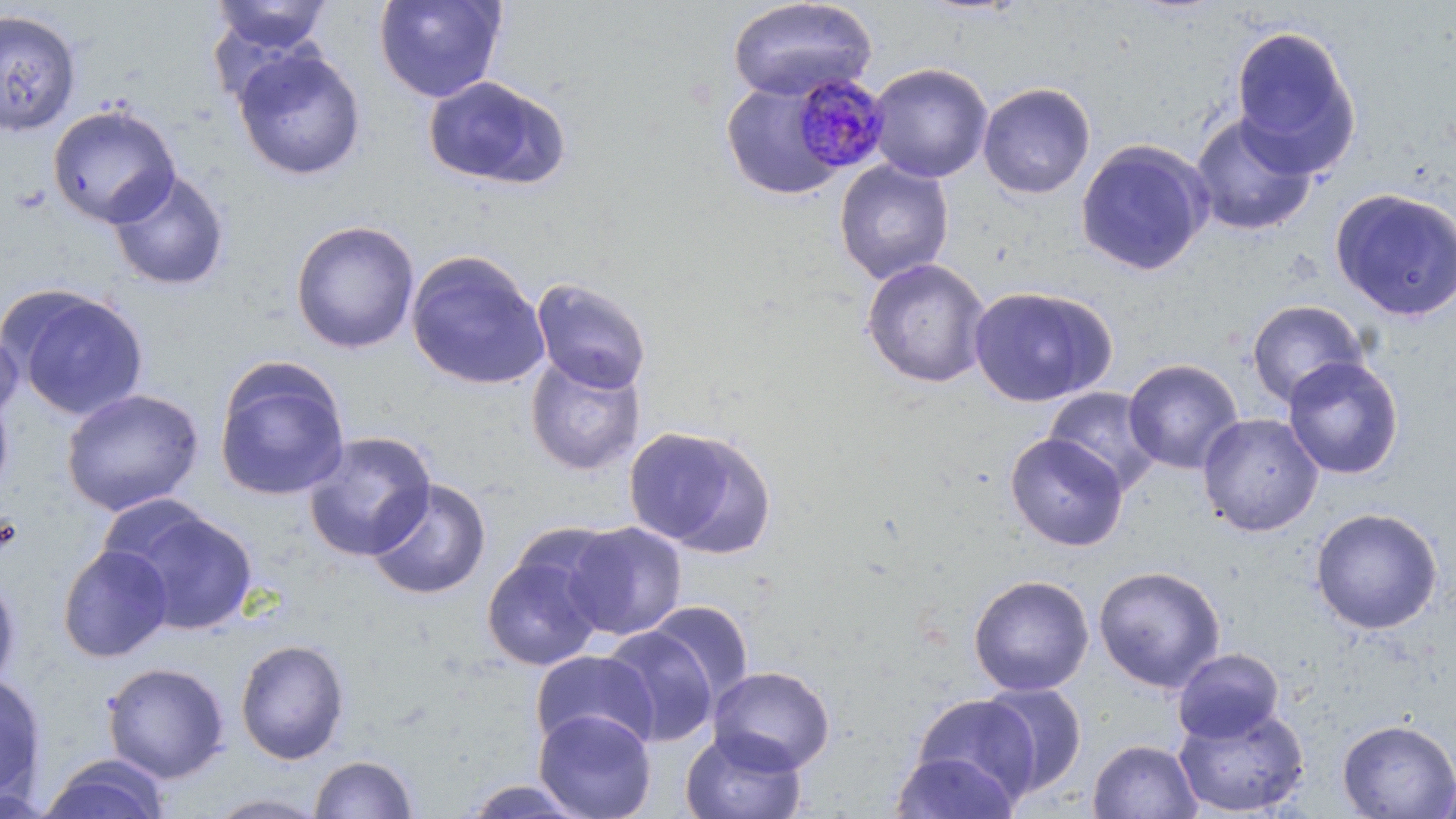

{
  "slide_level_diagnosis": "Plasmodium malariae",
  "image_size": "1456×819 pixels",
  "plasmodium_malariae_infected_red_blood_cell_locations": "approximate bounding boxes as (x1, y1, x2, y2) in pixels: (789, 71, 890, 175)",
  "field_of_view": "one of a larger specimen",
  "uninfected_red_blood_cell_locations": "approximate bounding boxes as (x1, y1, x2, y2) in pixels: (374, 0, 506, 103), (726, 0, 878, 102), (209, 1, 333, 55), (0, 10, 81, 136), (1229, 23, 1361, 174), (232, 46, 367, 181), (868, 63, 993, 183), (421, 75, 570, 191), (721, 79, 846, 201), (977, 82, 1096, 199), (47, 104, 180, 228), (1190, 113, 1318, 237), (1075, 139, 1213, 276), (833, 160, 955, 284), (108, 168, 230, 291), (1330, 188, 1456, 322), (290, 220, 421, 354), (406, 250, 549, 391), (860, 257, 992, 388), (530, 278, 652, 395), (4, 285, 150, 421), (967, 285, 1116, 407), (1246, 299, 1367, 408), (0, 321, 23, 429), (525, 354, 646, 476), (1282, 356, 1404, 480), (213, 358, 350, 501), (1123, 359, 1243, 474), (0, 386, 14, 500), (61, 387, 204, 516), (1043, 387, 1162, 494), (1197, 413, 1323, 536), (623, 424, 775, 556), (302, 431, 437, 561), (1005, 433, 1128, 551), (366, 478, 492, 601), (106, 502, 259, 636), (1311, 507, 1442, 635), (563, 520, 688, 641), (57, 544, 173, 663), (481, 548, 608, 672), (1093, 565, 1226, 693), (0, 568, 22, 693), (968, 574, 1094, 696), (646, 600, 755, 705), (600, 626, 720, 747), (234, 639, 351, 765), (1172, 648, 1285, 743), (529, 650, 658, 754), (101, 661, 230, 782), (708, 665, 836, 773), (0, 672, 48, 803), (978, 681, 1087, 797), (909, 694, 1041, 807), (1173, 705, 1309, 817), (533, 709, 657, 819), (1337, 719, 1456, 818), (679, 728, 806, 819), (1088, 739, 1202, 819), (889, 750, 1020, 819), (40, 754, 170, 819), (309, 754, 419, 818), (1436, 769, 1456, 818), (456, 779, 594, 818), (203, 791, 332, 818)",
  "modality": "light microscopy",
  "magnification": "1000x",
  "stain": "May-Grünwald-Giemsa",
  "preparation": "thin blood film"
}